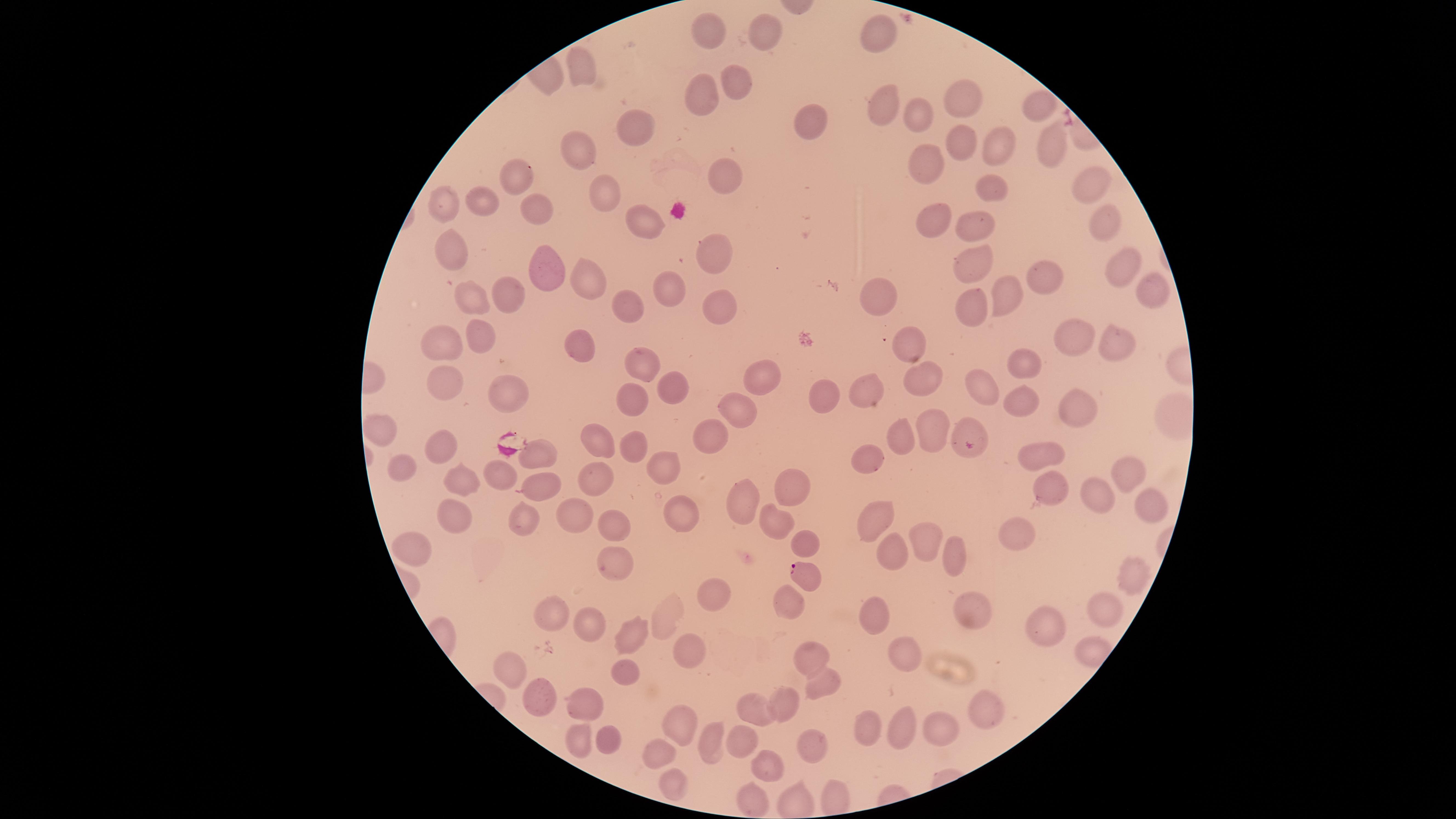

{
  "stain": "Giemsa",
  "capture": "smartphone photograph through the microscope eyepiece",
  "uninfected_red_blood_cells": "approximate marker points as (x, y) in pixels: (760, 26), (707, 28), (874, 34), (582, 68), (736, 84), (700, 92), (962, 96), (882, 98), (1036, 113), (921, 116), (816, 122), (634, 130), (963, 139), (992, 142), (1047, 145), (584, 153), (929, 165), (519, 173), (727, 180), (1087, 186), (984, 192), (610, 196), (490, 200), (444, 202), (538, 207), (932, 213), (1099, 219), (640, 220), (973, 223), (455, 248), (712, 250), (969, 258), (545, 266), (1118, 270), (585, 275), (1054, 278), (510, 291), (1150, 291), (669, 292), (1004, 294), (466, 301), (629, 301), (878, 301), (972, 303), (721, 305), (482, 336), (1074, 336), (1118, 337), (441, 342), (908, 342), (584, 344), (1024, 358), (645, 361), (765, 371), (922, 377), (440, 383), (669, 384), (983, 388), (501, 389), (861, 389), (825, 393), (1019, 394), (635, 399), (1077, 409), (735, 410), (388, 430), (967, 430), (933, 432), (709, 434), (599, 442), (901, 443), (444, 445), (636, 449), (537, 451), (1044, 451), (870, 458), (405, 466), (1131, 469), (667, 471), (496, 475), (596, 478), (461, 483), (538, 483), (797, 486), (1055, 492), (1100, 498), (745, 499), (1156, 504), (681, 512), (456, 514), (571, 514), (521, 517), (877, 519), (776, 520), (616, 524), (1023, 527), (416, 538), (925, 538), (806, 541), (891, 549), (955, 556), (612, 561), (1129, 576), (718, 592), (789, 601), (978, 606), (1103, 608), (877, 609), (555, 612), (592, 624), (657, 624), (1048, 624), (632, 636), (689, 650), (909, 651), (811, 656), (508, 664), (621, 673), (822, 687), (788, 702), (538, 703), (589, 703), (753, 710), (986, 711), (672, 724), (905, 725), (944, 726), (871, 727), (609, 736), (580, 737), (741, 742), (809, 744), (709, 745), (656, 757), (773, 765), (671, 787), (758, 800)",
  "parasitized_red_blood_cells": "approximate marker points as (x, y) in pixels: (801, 573)",
  "visible_region": "circular",
  "preparation": "thin blood film",
  "image_size": "1456×819 pixels",
  "species": "Plasmodium falciparum",
  "field_of_view": "single",
  "presence": "malaria parasites detected"
}